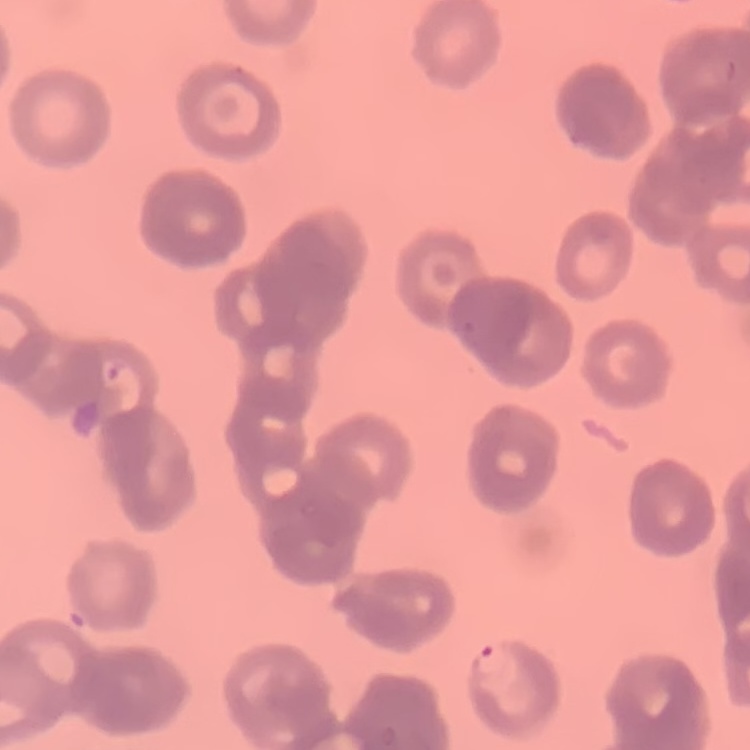
red_blood_cell_morphology: rouleaux formation
stain: Field's or Giemsa
image_type: one tile cut from a larger photomicrograph
preparation: thin blood smear